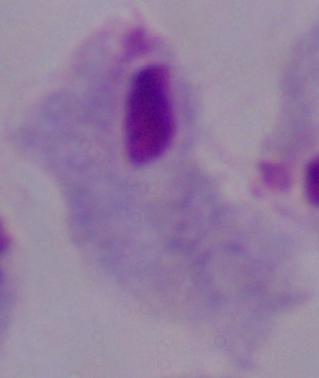

A trichomonad is seen. Photomicrograph. Captured at 1000x magnification.